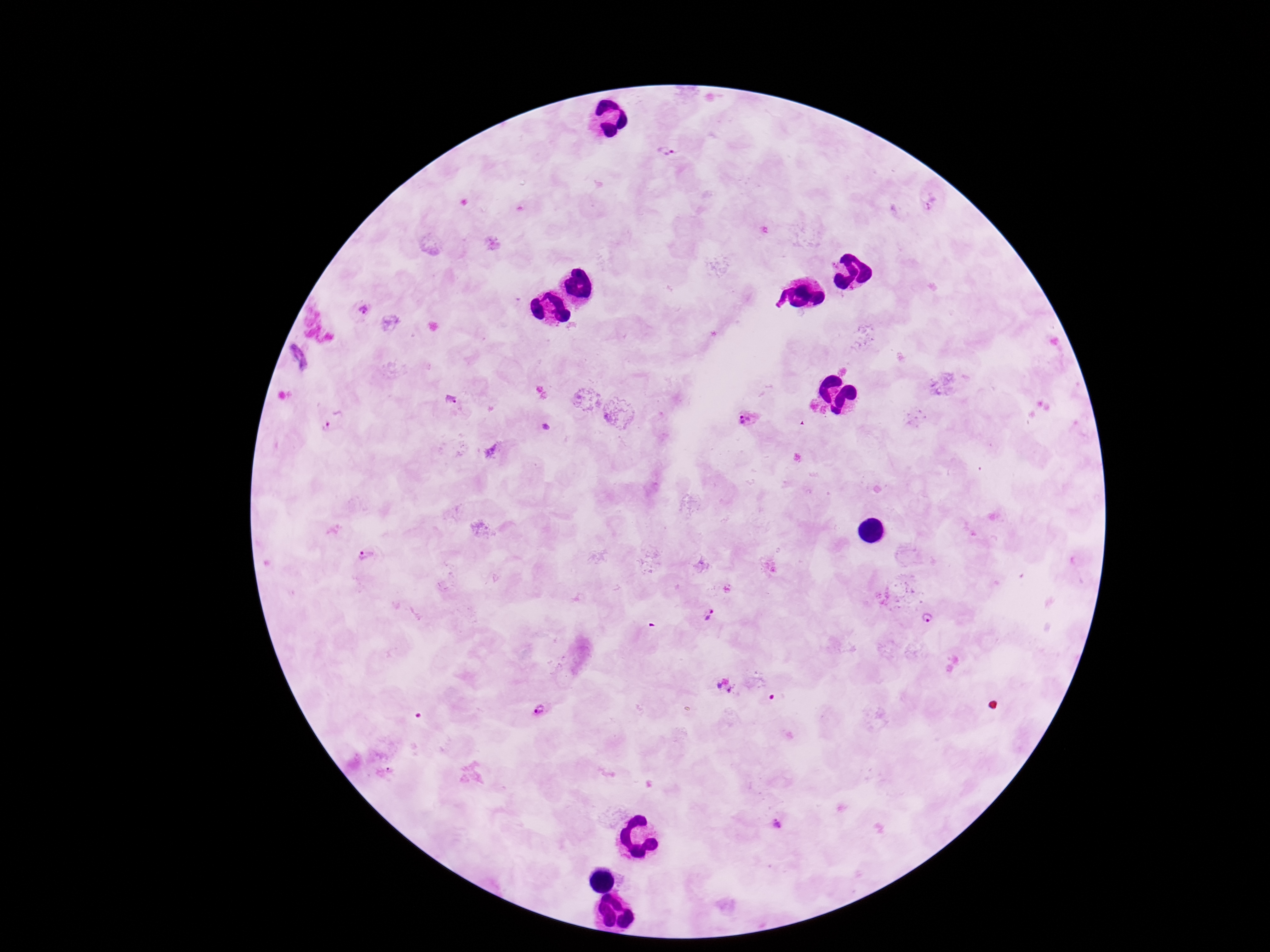
Approximate centers as [x, y] in pixels. Plasmodium parasite locations: [667, 152], [929, 201], [362, 309], [296, 358], [453, 400], [335, 417], [749, 417], [367, 553], [708, 614], [929, 618], [540, 710], [778, 824]. 100x magnification. Image is 1270×952 pixels. Patient malaria status: positive. Single field of view. Thick blood smear. Giemsa stain. Smartphone photograph taken through the microscope eyepiece.